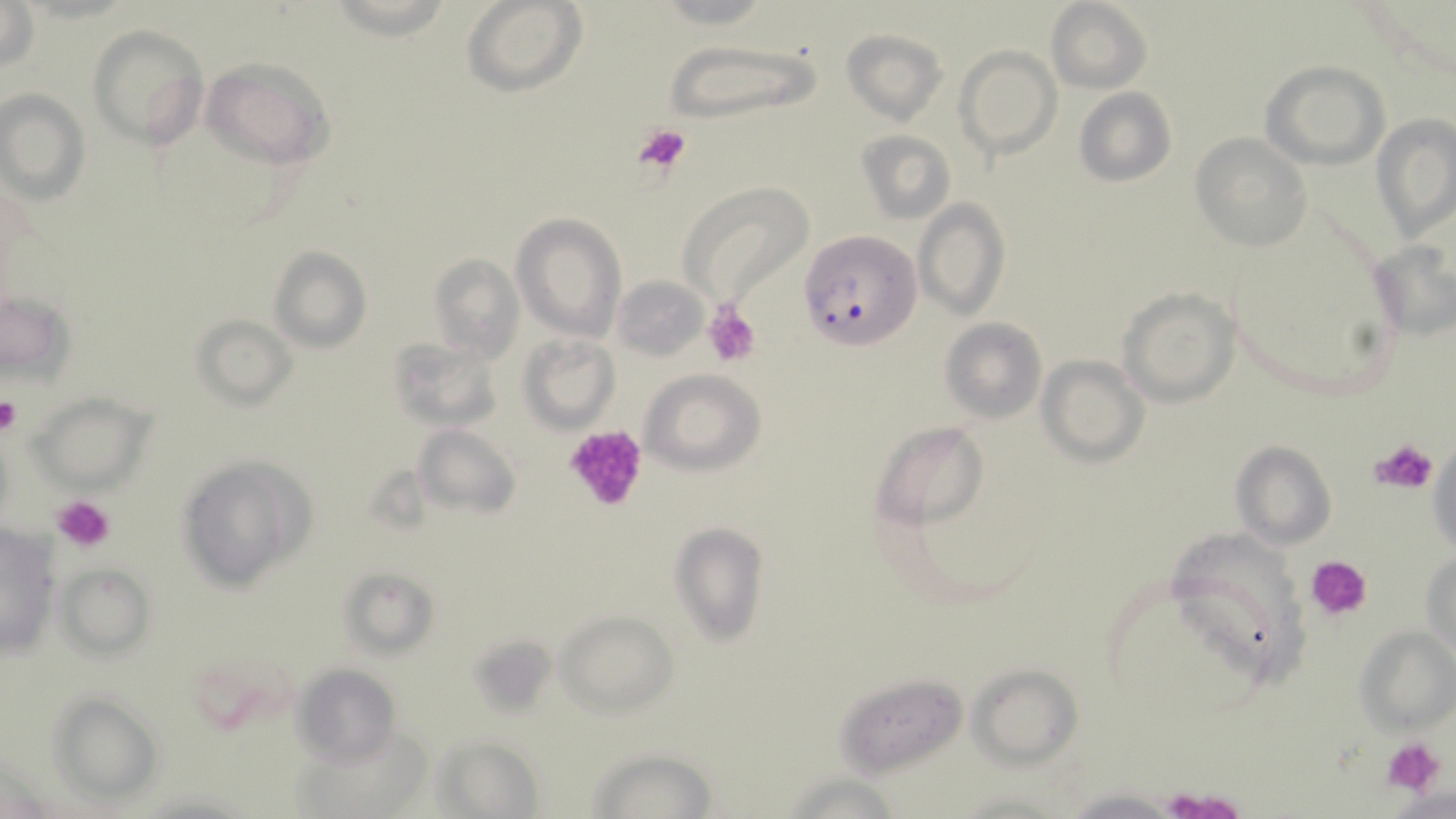
slide-level diagnosis = Plasmodium falciparum
platelet locations = approximate bounding boxes as named x1/y1/x2/y2 corners in pixels: (x1=631, y1=121, x2=693, y2=178), (x1=703, y1=304, x2=760, y2=365), (x1=0, y1=397, x2=20, y2=436), (x1=560, y1=423, x2=650, y2=514), (x1=1369, y1=436, x2=1438, y2=497), (x1=53, y1=494, x2=116, y2=553), (x1=1307, y1=556, x2=1374, y2=622), (x1=1381, y1=735, x2=1448, y2=799), (x1=1162, y1=787, x2=1245, y2=818)
field of view = one of a larger specimen
modality = optical microscopy
Plasmodium falciparum-infected red blood cell locations = approximate bounding boxes as named x1/y1/x2/y2 corners in pixels: (x1=800, y1=229, x2=920, y2=352)
stain = May-Grünwald-Giemsa
preparation = thin blood film
image size = 1456×819 pixels
magnification = 1000x
uninfected red blood cell locations = approximate bounding boxes as named x1/y1/x2/y2 corners in pixels: (x1=1, y1=1, x2=40, y2=73), (x1=460, y1=1, x2=586, y2=96), (x1=1045, y1=1, x2=1154, y2=93), (x1=88, y1=24, x2=208, y2=147), (x1=843, y1=30, x2=945, y2=125), (x1=659, y1=39, x2=820, y2=128), (x1=954, y1=46, x2=1062, y2=160), (x1=201, y1=57, x2=334, y2=169), (x1=1261, y1=61, x2=1389, y2=169), (x1=1073, y1=88, x2=1177, y2=188), (x1=0, y1=89, x2=90, y2=203), (x1=1372, y1=113, x2=1456, y2=242), (x1=855, y1=130, x2=955, y2=225), (x1=1192, y1=132, x2=1312, y2=253), (x1=679, y1=182, x2=811, y2=305), (x1=915, y1=199, x2=1008, y2=320), (x1=512, y1=213, x2=626, y2=341), (x1=1368, y1=236, x2=1455, y2=346), (x1=268, y1=246, x2=371, y2=353), (x1=426, y1=252, x2=526, y2=363), (x1=611, y1=277, x2=709, y2=363), (x1=1119, y1=287, x2=1239, y2=407), (x1=2, y1=289, x2=75, y2=386), (x1=194, y1=313, x2=297, y2=410), (x1=940, y1=319, x2=1046, y2=421), (x1=518, y1=334, x2=620, y2=433), (x1=1036, y1=355, x2=1149, y2=465), (x1=638, y1=368, x2=766, y2=475), (x1=31, y1=392, x2=153, y2=494), (x1=872, y1=421, x2=988, y2=531), (x1=411, y1=424, x2=521, y2=522), (x1=1427, y1=434, x2=1455, y2=565), (x1=1231, y1=440, x2=1336, y2=549), (x1=177, y1=454, x2=314, y2=592), (x1=670, y1=524, x2=769, y2=645), (x1=0, y1=525, x2=63, y2=664), (x1=1161, y1=530, x2=1310, y2=685), (x1=1422, y1=547, x2=1455, y2=659), (x1=57, y1=563, x2=155, y2=660), (x1=338, y1=568, x2=440, y2=658), (x1=558, y1=610, x2=677, y2=714), (x1=1358, y1=625, x2=1455, y2=733), (x1=464, y1=633, x2=558, y2=721), (x1=291, y1=664, x2=403, y2=767), (x1=969, y1=664, x2=1083, y2=766), (x1=834, y1=667, x2=969, y2=776), (x1=46, y1=692, x2=160, y2=803), (x1=433, y1=734, x2=545, y2=817), (x1=586, y1=747, x2=718, y2=819), (x1=781, y1=771, x2=909, y2=819), (x1=1063, y1=787, x2=1185, y2=818)